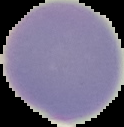

Result: negative for malaria parasites. From a thin blood smear. Image is 124×127 pixels. The area outside the segmented cell region is set to black.